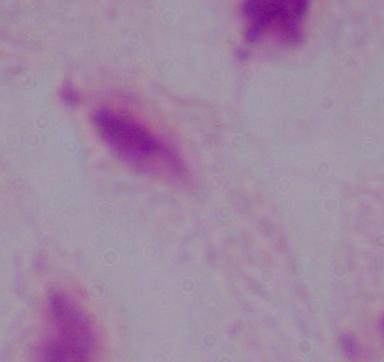

modality = micrograph
magnification = 1000x
identification = trichomonad